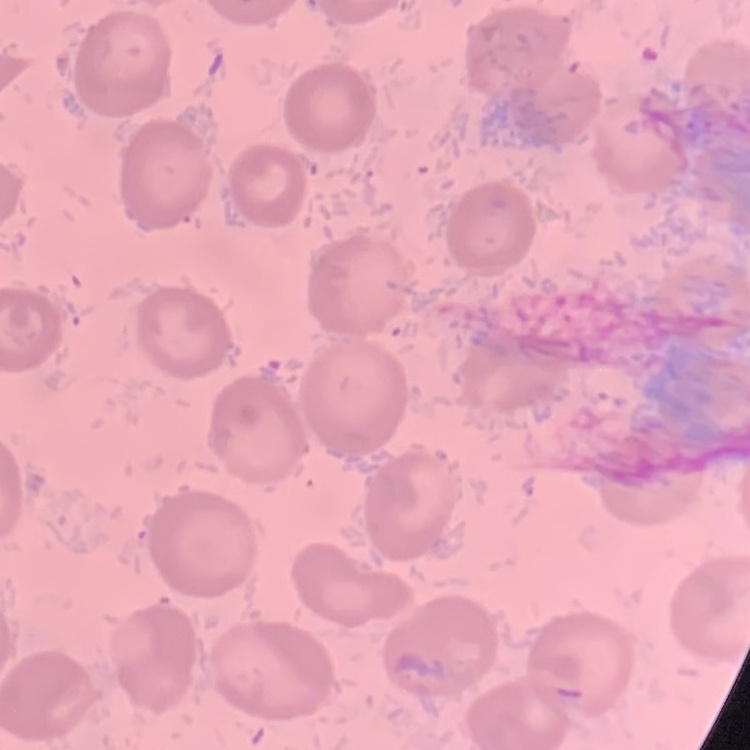

erythrocyte_morphology: no rouleaux formation
image_type: one tile cut from a larger photomicrograph
stain: Field's or Giemsa
preparation: thin blood smear